Assess the morphology of the red blood cells.
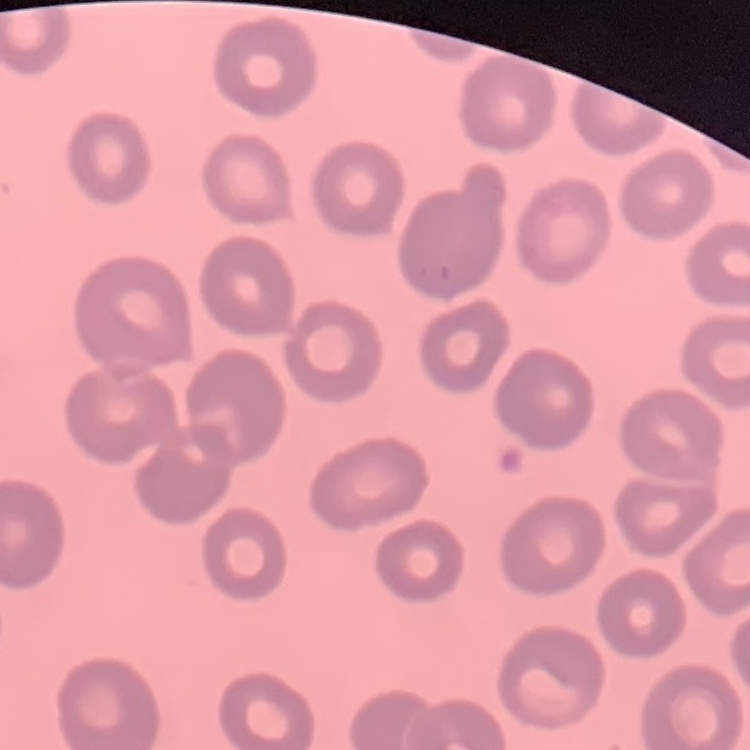
No rouleaux formation.

Summary:
  - Preparation: thin blood smear
  - Image type: one tile cut from a larger photomicrograph
  - Stain: Field's or Giemsa